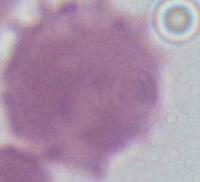
Summary:
  - Modality: photomicrograph
  - Magnification: 1000x
  - Identification: erythrocyte